State the preparation type.
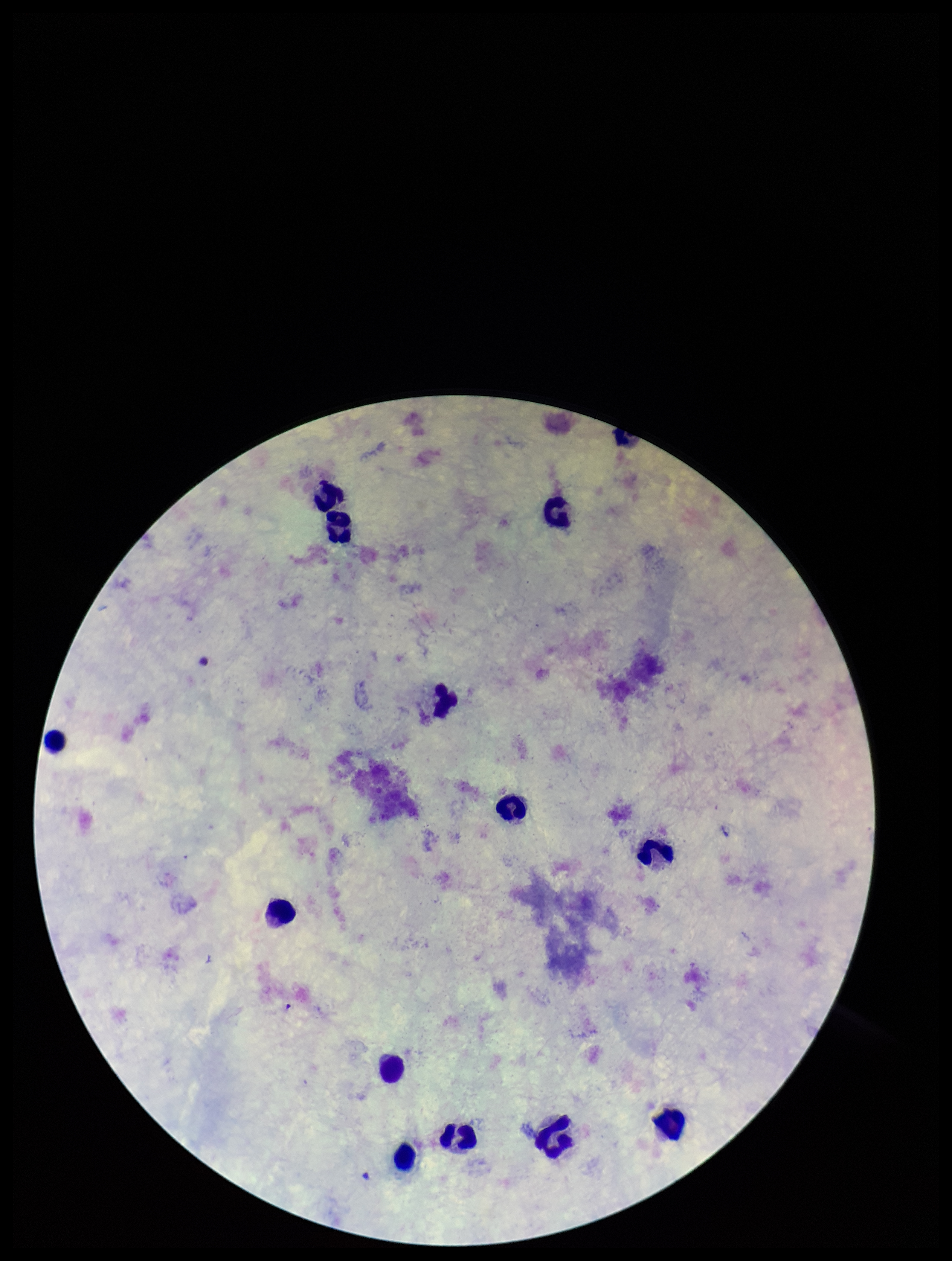
A thick smear.

image_size: 952×1261 pixels
stain: Giemsa
plasmodium_parasites: none seen
capture: smartphone photograph through the microscope eyepiece
leukocyte_count: 13
patient_malaria_status: negative
parasite_count: 0
field_of_view: single